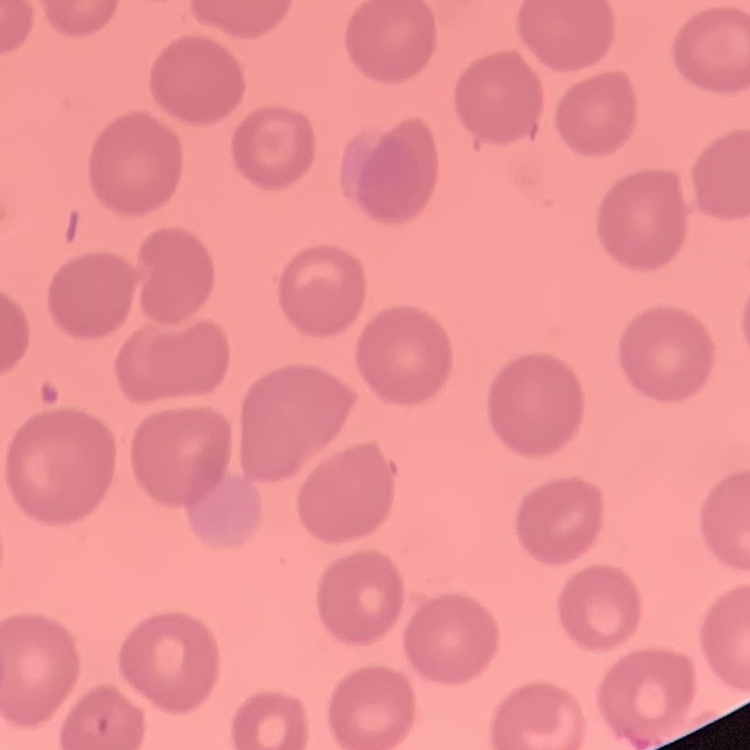
erythrocyte morphology = no rouleaux formation
preparation = thin peripheral smear
image type = one tile cut from a larger photomicrograph
stain = Field's or Giemsa